Report the malaria status of this cell.
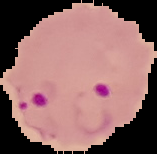
It is parasitized.

{
  "image_size": "157×154 pixels",
  "preparation": "thin blood film",
  "image_type": "cell region segmented out of the field of view; surrounding area masked to black"
}